Locate every blood parasite and identify its species.
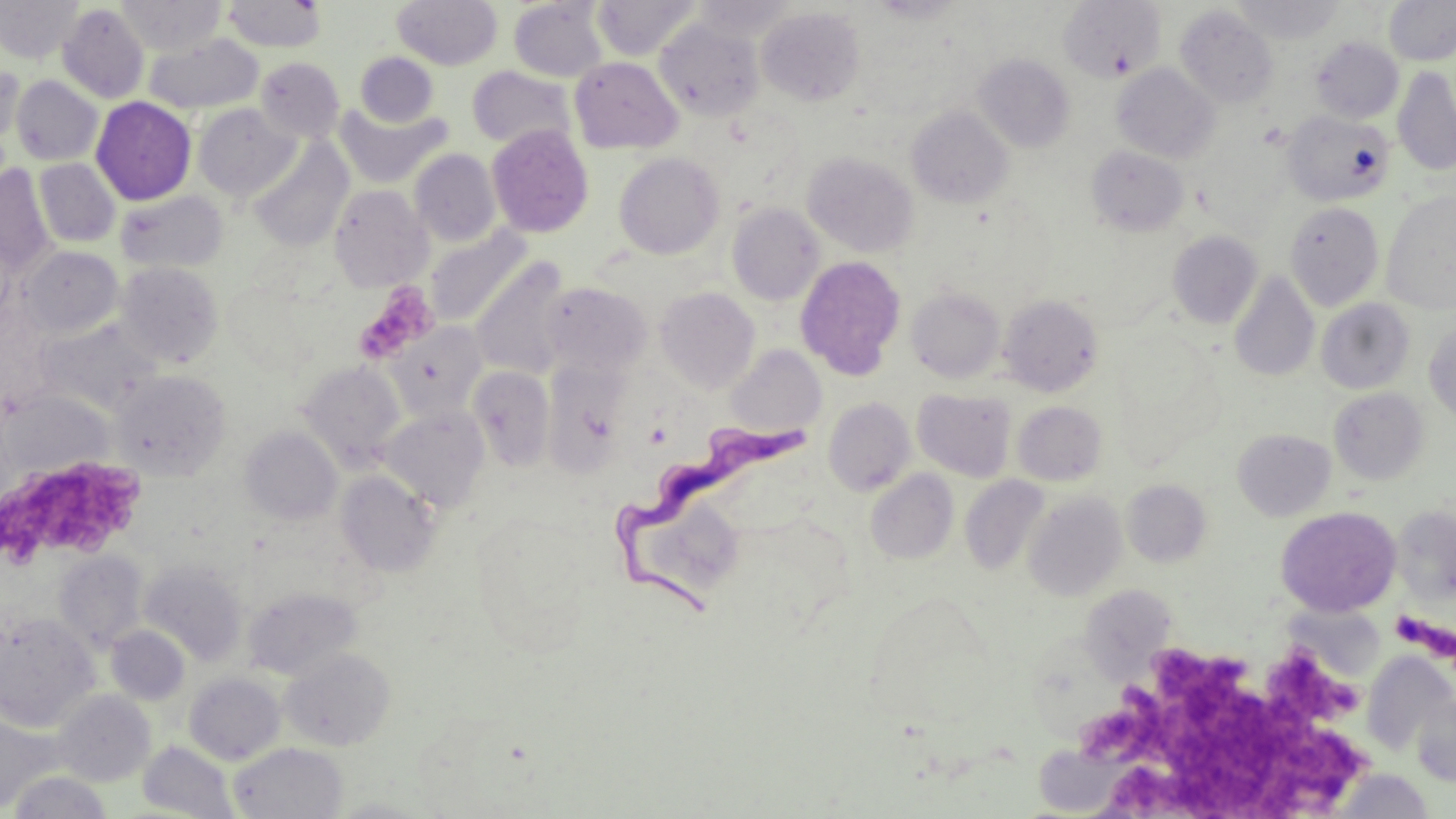

Approximate bounding boxes as (x1,y1)-(x2,y2) corner pairs in pixels.
Trypanosoma brucei: (611,415)-(812,625).
No Plasmodium falciparum, Plasmodium ovale, Plasmodium malariae, Plasmodium vivax, or Babesia divergens observed.

Uninfected red blood cell locations: (0,0)-(83,64), (116,0)-(226,54), (221,0)-(328,52), (392,0)-(502,69), (592,0)-(701,61), (691,0)-(801,40), (868,0)-(967,23), (1058,0)-(1166,83), (1231,0)-(1345,43), (1384,0)-(1456,65), (509,1)-(608,82), (57,3)-(150,104), (1175,5)-(1278,109), (757,7)-(865,106), (654,18)-(764,121), (144,33)-(264,114), (1311,37)-(1403,123), (355,52)-(438,127), (974,54)-(1075,153), (569,56)-(683,154), (255,57)-(345,142), (0,63)-(24,148), (1112,63)-(1219,164), (467,66)-(577,151), (1393,67)-(1456,176), (11,75)-(102,165), (91,96)-(196,205), (193,103)-(299,201), (335,103)-(449,188), (906,106)-(1013,208), (1281,110)-(1395,206), (486,124)-(595,238), (249,140)-(353,251), (1086,146)-(1189,236), (410,148)-(501,246), (614,152)-(724,259), (802,152)-(919,257), (34,158)-(120,247), (0,164)-(56,276), (329,184)-(432,291), (1381,190)-(1456,314), (116,191)-(227,273), (1284,202)-(1384,311), (727,203)-(825,305), (425,226)-(532,329), (1167,231)-(1262,328), (20,246)-(123,336), (795,256)-(906,380), (470,257)-(572,380), (115,261)-(224,367), (1228,271)-(1320,382), (542,282)-(653,376), (655,286)-(760,392), (907,286)-(1006,383), (998,294)-(1103,396), (1316,299)-(1415,394), (1424,321)-(1456,424), (385,323)-(489,425), (724,345)-(826,439), (296,360)-(407,470), (542,362)-(631,477), (468,366)-(555,471), (110,368)-(231,480), (912,388)-(1017,481), (1329,388)-(1429,485), (824,398)-(916,495), (1012,401)-(1107,485), (379,405)-(491,513), (240,425)-(343,524), (1232,429)-(1336,521), (865,469)-(959,563), (335,470)-(441,578), (959,475)-(1051,577), (1122,479)-(1212,567), (1023,491)-(1127,601), (623,492)-(746,607), (1392,505)-(1456,606), (1276,507)-(1401,617), (54,551)-(148,652), (140,561)-(248,667), (1078,580)-(1174,686), (243,586)-(361,680), (1279,596)-(1388,684), (0,612)-(99,730), (106,625)-(191,705), (280,647)-(396,751), (1361,654)-(1454,757), (183,672)-(285,765), (53,690)-(156,787), (1412,693)-(1456,787), (0,715)-(63,812), (139,741)-(238,818), (1044,741)-(1117,816), (229,742)-(347,819), (1331,768)-(1436,817), (7,771)-(113,818), (327,797)-(437,818). Platelet locations: (359,280)-(438,361), (3,453)-(146,562), (1388,611)-(1435,648), (1153,639)-(1252,738), (1262,641)-(1362,726), (1095,687)-(1366,819). Slide-level diagnosis: Trypanosoma brucei. Light microscopy. Captured at 1000x magnification. May-Grünwald-Giemsa-stained preparation. Single field of view. Image is 1456×819 pixels. Thin blood film.